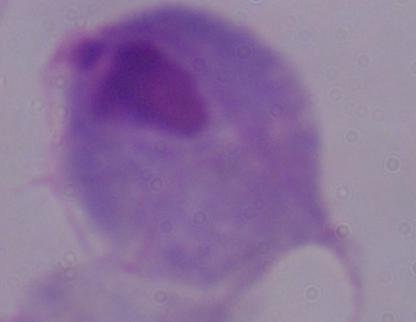

A trichomonad is seen. Micrograph. Captured at 1000x magnification.